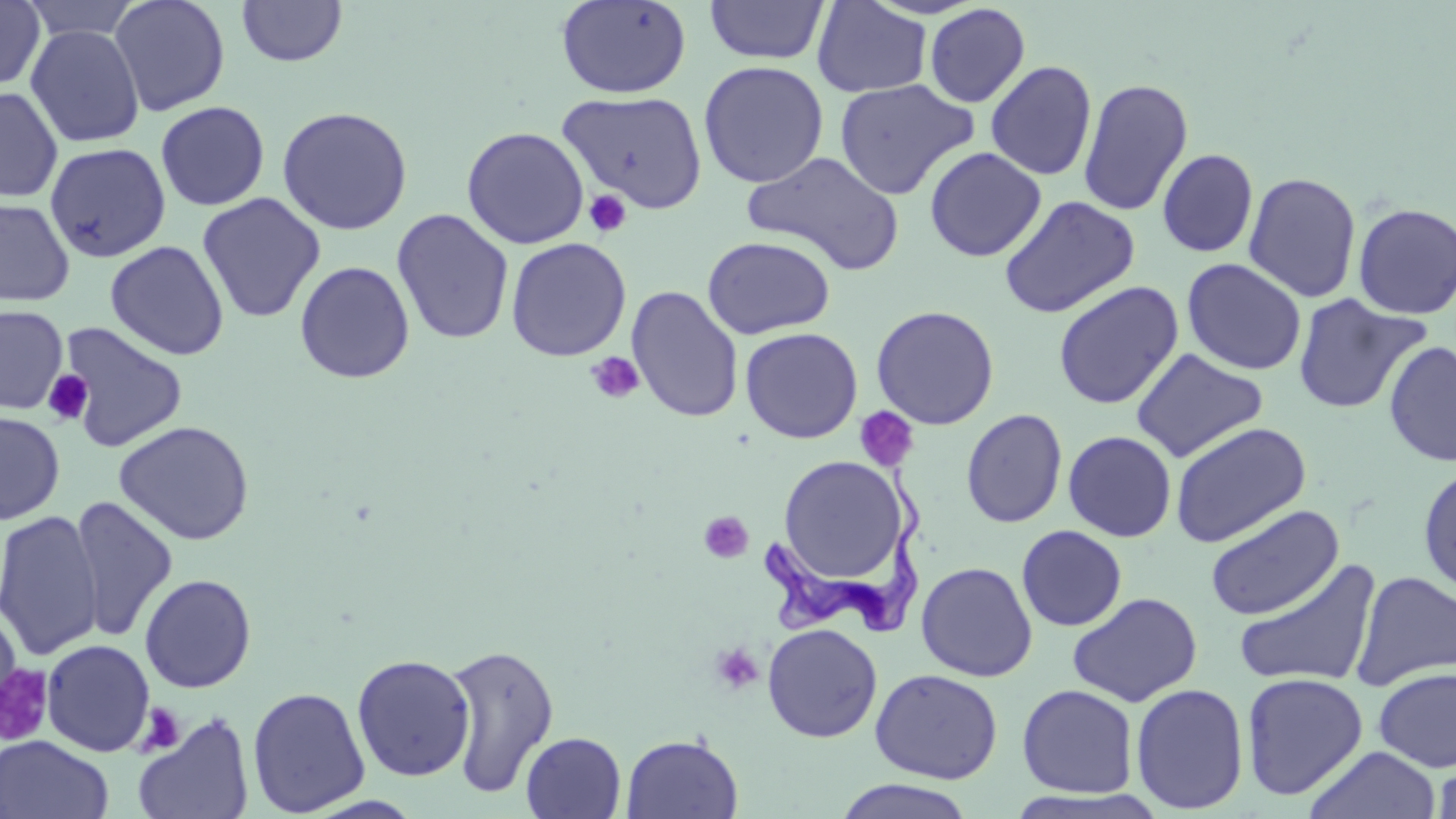

slide-level diagnosis = Trypanosoma brucei
preparation = thin blood smear
Trypanosoma brucei locations = approximate bounding boxes as named x1/y1/x2/y2 corners in pixels: (x1=761, y1=466, x2=922, y2=637)
uninfected red blood cell locations = approximate bounding boxes as named x1/y1/x2/y2 corners in pixels: (x1=0, y1=0, x2=46, y2=91), (x1=21, y1=0, x2=142, y2=42), (x1=109, y1=0, x2=231, y2=117), (x1=236, y1=0, x2=348, y2=67), (x1=555, y1=0, x2=692, y2=99), (x1=704, y1=0, x2=829, y2=64), (x1=812, y1=1, x2=932, y2=97), (x1=924, y1=3, x2=1030, y2=108), (x1=25, y1=24, x2=145, y2=147), (x1=39, y1=24, x2=155, y2=259), (x1=698, y1=60, x2=829, y2=188), (x1=986, y1=60, x2=1097, y2=180), (x1=833, y1=78, x2=979, y2=200), (x1=1077, y1=78, x2=1194, y2=217), (x1=0, y1=86, x2=63, y2=203), (x1=556, y1=90, x2=707, y2=212), (x1=155, y1=100, x2=270, y2=211), (x1=276, y1=106, x2=413, y2=235), (x1=462, y1=126, x2=589, y2=249), (x1=44, y1=142, x2=171, y2=262), (x1=924, y1=146, x2=1047, y2=262), (x1=1157, y1=148, x2=1259, y2=258), (x1=743, y1=150, x2=905, y2=276), (x1=1243, y1=171, x2=1362, y2=303), (x1=197, y1=193, x2=325, y2=323), (x1=998, y1=195, x2=1140, y2=319), (x1=0, y1=198, x2=75, y2=307), (x1=1352, y1=202, x2=1456, y2=320), (x1=391, y1=209, x2=514, y2=345), (x1=701, y1=235, x2=835, y2=339), (x1=506, y1=237, x2=631, y2=361), (x1=105, y1=240, x2=229, y2=360), (x1=1181, y1=258, x2=1306, y2=376), (x1=294, y1=260, x2=415, y2=384), (x1=1052, y1=280, x2=1184, y2=410), (x1=626, y1=286, x2=744, y2=423), (x1=1292, y1=293, x2=1430, y2=415), (x1=870, y1=304, x2=1000, y2=430), (x1=0, y1=305, x2=68, y2=414), (x1=55, y1=321, x2=189, y2=453), (x1=740, y1=327, x2=863, y2=444), (x1=1383, y1=341, x2=1456, y2=468), (x1=1131, y1=348, x2=1268, y2=462), (x1=961, y1=409, x2=1068, y2=528), (x1=0, y1=410, x2=65, y2=525), (x1=114, y1=420, x2=254, y2=545), (x1=1169, y1=421, x2=1312, y2=547), (x1=1063, y1=430, x2=1177, y2=541), (x1=777, y1=456, x2=907, y2=586), (x1=1417, y1=463, x2=1456, y2=598), (x1=69, y1=495, x2=178, y2=643), (x1=1204, y1=504, x2=1344, y2=620), (x1=1, y1=509, x2=103, y2=661), (x1=1017, y1=525, x2=1127, y2=631), (x1=1232, y1=558, x2=1383, y2=689), (x1=916, y1=561, x2=1038, y2=682), (x1=1350, y1=570, x2=1456, y2=692), (x1=139, y1=573, x2=257, y2=693), (x1=1068, y1=591, x2=1203, y2=707), (x1=0, y1=612, x2=22, y2=722), (x1=762, y1=623, x2=882, y2=743), (x1=40, y1=639, x2=156, y2=757), (x1=444, y1=641, x2=560, y2=798), (x1=352, y1=653, x2=475, y2=782), (x1=0, y1=665, x2=53, y2=746), (x1=1373, y1=667, x2=1456, y2=772), (x1=870, y1=668, x2=1003, y2=784), (x1=1240, y1=672, x2=1368, y2=800), (x1=1130, y1=682, x2=1249, y2=814), (x1=1016, y1=683, x2=1139, y2=798), (x1=247, y1=686, x2=370, y2=817), (x1=133, y1=712, x2=255, y2=819), (x1=521, y1=732, x2=626, y2=818), (x1=621, y1=733, x2=744, y2=818), (x1=0, y1=735, x2=114, y2=819), (x1=1304, y1=746, x2=1441, y2=819), (x1=1432, y1=754, x2=1456, y2=819), (x1=832, y1=778, x2=978, y2=818)
image size = 1456×819 pixels
platelet locations = approximate bounding boxes as named x1/y1/x2/y2 corners in pixels: (x1=584, y1=189, x2=632, y2=237), (x1=585, y1=351, x2=645, y2=404), (x1=44, y1=370, x2=93, y2=425), (x1=854, y1=407, x2=919, y2=474), (x1=699, y1=510, x2=754, y2=563), (x1=708, y1=641, x2=765, y2=696), (x1=137, y1=702, x2=185, y2=756)
magnification = 1000x
field of view = single
stain = May-Grünwald-Giemsa
modality = light microscopy